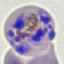

Result: malaria parasites detected. Thin blood smear. Giemsa stain. Acquired by smartphone through the microscope eyepiece. Automatically extracted cell patch, resized to 64 × 64 pixels.